Locate every white blood cell.
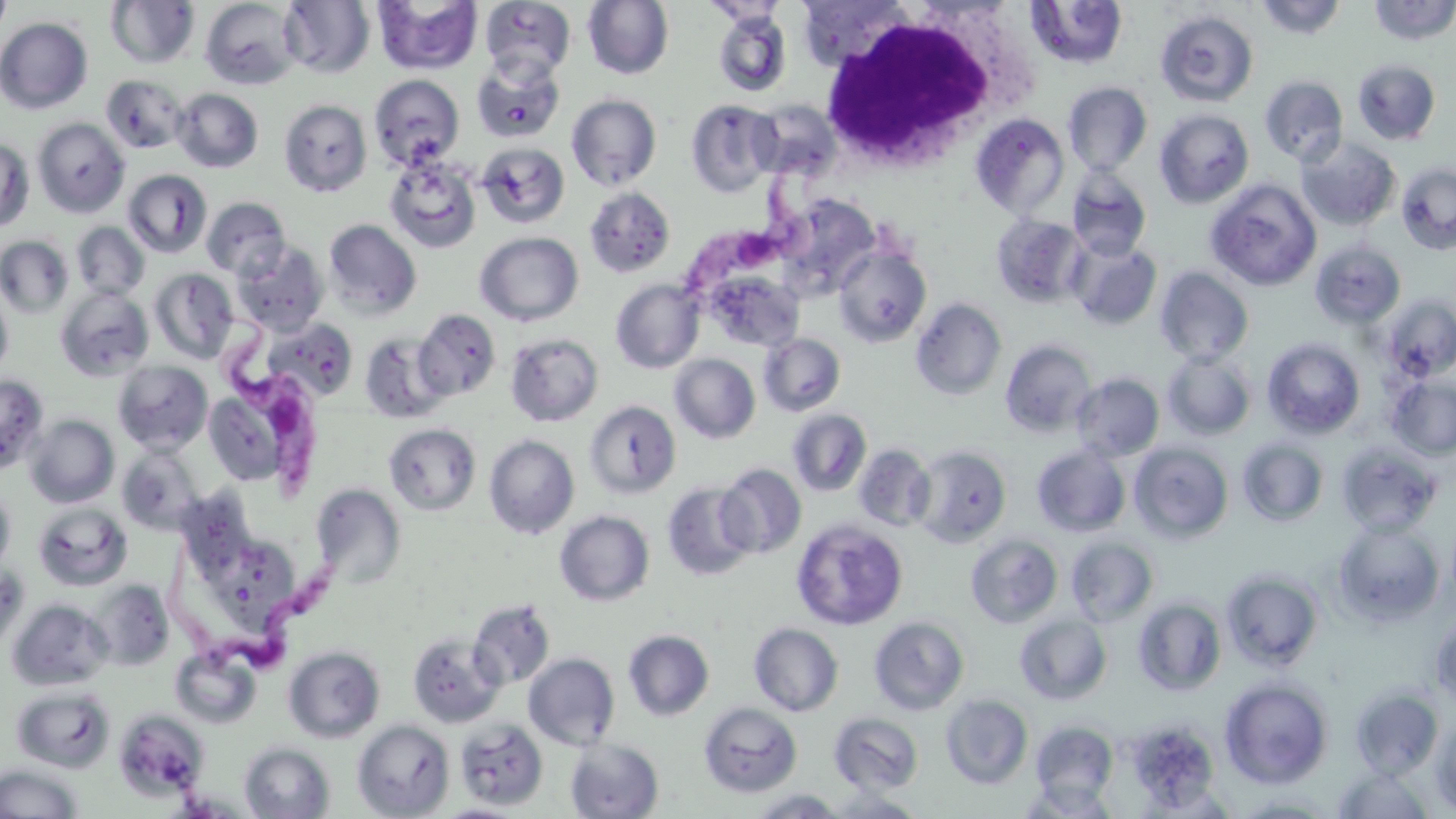
Approximate bounding boxes as [x1, y1, x2, y2] in pixels.
White blood cells: [818, 8, 1027, 166].

slide_level_diagnosis: Trypanosoma brucei
stain: May-Grünwald-Giemsa
image_size: 1456×819 pixels
modality: light microscopy
trypanosoma_brucei_locations: 'approximate bounding boxes as [x1, y1, x2, y2] in pixels: [684, 160, 828, 293], [212, 313, 331, 498], [165, 533, 351, 672]'
preparation: thin blood smear
magnification: 1000x
uninfected_red_blood_cell_locations: 'approximate bounding boxes as [x1, y1, x2, y2] in pixels: [0, 0, 12, 44], [201, 0, 302, 90], [372, 0, 483, 76], [480, 0, 576, 81], [583, 0, 674, 79], [797, 0, 914, 71], [1255, 0, 1348, 40], [1367, 0, 1456, 45], [105, 1, 200, 68], [278, 1, 375, 79], [1025, 1, 1129, 70], [712, 9, 792, 98], [1156, 10, 1259, 107], [1, 17, 93, 114], [471, 54, 566, 144], [1352, 59, 1441, 145], [101, 74, 189, 154], [368, 74, 465, 171], [1259, 75, 1349, 166], [1063, 81, 1153, 176], [172, 88, 263, 172], [566, 93, 662, 191], [278, 99, 371, 196], [685, 99, 779, 197], [748, 99, 841, 181], [1154, 109, 1254, 208], [970, 113, 1070, 219], [32, 117, 130, 218], [1296, 136, 1401, 231], [0, 139, 34, 231], [476, 142, 570, 228], [385, 156, 481, 253], [1396, 162, 1456, 255], [1067, 167, 1151, 261], [123, 169, 214, 257], [1204, 179, 1322, 291], [584, 186, 676, 278], [778, 195, 881, 298], [201, 197, 291, 280], [992, 214, 1089, 309], [324, 219, 422, 320], [72, 222, 149, 300], [475, 232, 584, 326], [0, 235, 73, 318], [1067, 238, 1162, 330], [1310, 240, 1406, 330], [233, 242, 329, 336], [834, 245, 932, 348], [1155, 267, 1254, 365], [150, 268, 239, 363], [704, 271, 804, 352], [611, 279, 705, 373], [0, 285, 13, 380], [55, 287, 153, 382], [1381, 295, 1456, 382], [911, 297, 1007, 400], [413, 309, 501, 401], [262, 317, 359, 403], [358, 331, 450, 424], [505, 333, 604, 426], [759, 333, 846, 416], [1262, 338, 1365, 438], [1000, 339, 1097, 437], [1163, 350, 1257, 440], [669, 354, 760, 443], [113, 360, 213, 454], [1071, 373, 1164, 462], [0, 374, 48, 472], [1387, 376, 1456, 460], [204, 387, 290, 487], [584, 400, 682, 499], [787, 409, 872, 496], [25, 415, 120, 508], [384, 423, 482, 515], [484, 434, 579, 539], [1238, 439, 1329, 527], [1129, 442, 1234, 543], [1337, 442, 1442, 537], [116, 443, 204, 535], [853, 444, 936, 531], [912, 444, 1012, 548], [1031, 444, 1131, 538], [715, 463, 806, 559], [662, 482, 758, 581], [311, 484, 406, 588], [0, 485, 16, 575], [184, 486, 259, 576], [33, 502, 133, 591], [554, 510, 655, 606], [791, 518, 908, 630], [1332, 518, 1445, 626], [965, 533, 1063, 628], [209, 534, 299, 629], [1066, 536, 1159, 626], [0, 562, 28, 651], [1220, 568, 1324, 671], [87, 579, 175, 671], [1133, 597, 1227, 696], [7, 598, 112, 691], [468, 599, 556, 690], [1429, 612, 1456, 709], [1015, 613, 1112, 704], [869, 616, 970, 716], [749, 623, 844, 716], [623, 630, 714, 721], [407, 633, 506, 728], [283, 644, 506, 737], [283, 645, 385, 743], [170, 646, 262, 728], [523, 652, 620, 750], [1220, 677, 1333, 789], [12, 685, 115, 773], [1349, 687, 1443, 778], [941, 694, 1034, 789], [699, 702, 802, 798], [114, 710, 208, 801], [829, 712, 924, 795], [1432, 716, 1456, 815], [1126, 717, 1221, 813], [454, 719, 549, 810], [352, 720, 455, 819], [1030, 720, 1119, 806], [564, 738, 664, 818], [240, 742, 335, 819], [0, 763, 83, 819], [1332, 765, 1437, 817], [1021, 779, 1118, 818], [747, 788, 849, 818], [821, 789, 928, 818], [1227, 793, 1343, 817], [431, 803, 528, 818]'
field_of_view: single